Name the parasite shown.
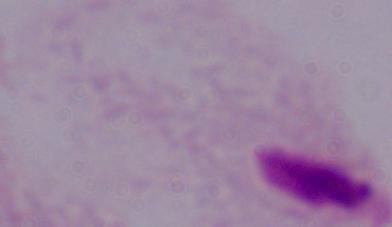

This is a trichomonad.

Summary:
  - Modality: photomicrograph
  - Magnification: 1000x